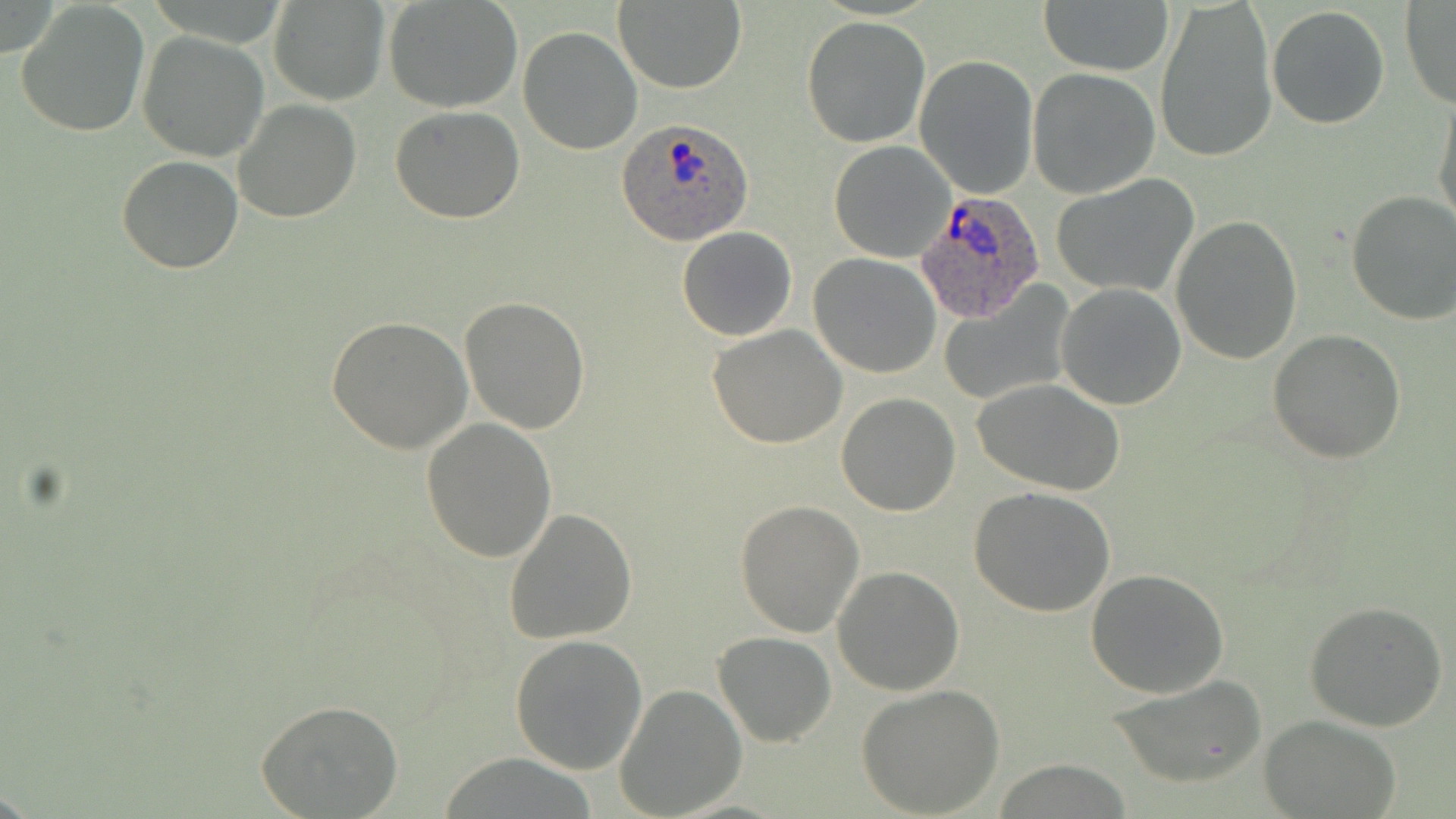

Summary:
  - Coordinate format: approximate bounding boxes as [x1, y1, x2, y2] in pixels
  - Uninfected red blood cell locations: [268, 0, 390, 105], [384, 0, 524, 113], [1155, 0, 1277, 163], [15, 1, 151, 138], [613, 1, 745, 92], [1039, 1, 1172, 77], [1400, 2, 1456, 109], [1266, 5, 1391, 130], [801, 16, 931, 149], [517, 27, 641, 155], [137, 33, 268, 161], [916, 56, 1039, 199], [1028, 69, 1160, 197], [1434, 95, 1456, 235], [234, 100, 362, 223], [391, 107, 525, 223], [829, 140, 957, 262], [116, 155, 244, 274], [1053, 175, 1199, 298], [1346, 190, 1456, 325], [1170, 216, 1302, 363], [677, 227, 798, 342], [809, 253, 942, 377], [937, 281, 1077, 407], [1056, 284, 1186, 410], [459, 297, 591, 433], [328, 316, 472, 453], [707, 324, 846, 449], [1268, 330, 1405, 464], [972, 378, 1127, 495], [837, 393, 960, 516], [422, 418, 557, 560], [968, 486, 1116, 616], [734, 499, 863, 636], [504, 509, 637, 645], [832, 565, 965, 696], [1084, 569, 1230, 699], [1303, 601, 1448, 733], [715, 630, 836, 746], [509, 634, 647, 776], [1107, 674, 1269, 787], [615, 684, 745, 817], [856, 685, 1005, 816], [254, 699, 404, 817], [1262, 715, 1402, 818]
  - Plasmodium ovale-infected red blood cell locations: [619, 119, 754, 247], [915, 189, 1046, 324]
  - Slide-level diagnosis: Plasmodium ovale
  - Preparation: thin blood smear
  - Modality: optical microscopy
  - Magnification: 1000x
  - Field of view: single
  - Stain: May-Grünwald-Giemsa
  - Image size: 1456×819 pixels